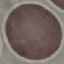 Malaria status: uninfected. Cell patch, automatically extracted from a larger field of view and resized to 64 × 64 pixels. Thin blood film. Photographed with a smartphone camera at the microscope eyepiece. Giemsa stain.